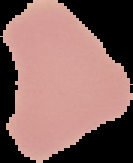
From a thin blood film. Malaria status: uninfected. Segmented cell region on a black background. Image is 133×163 pixels.